Outline platelets.
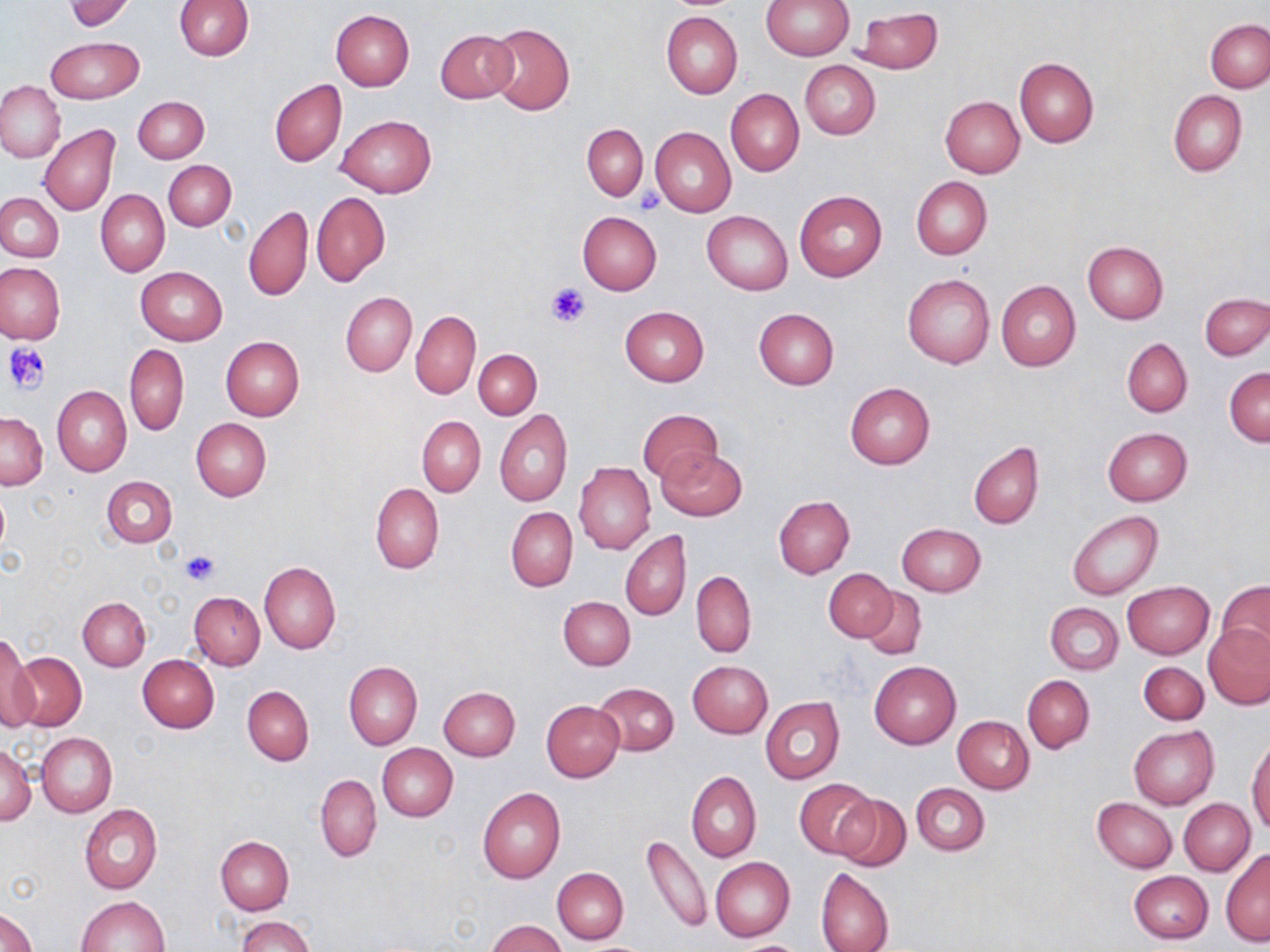

Approximate bounding boxes as (x1, y1, x2, y2) in pixels.
Platelets: (636, 191, 665, 215), (546, 284, 590, 330), (2, 343, 51, 394), (179, 549, 220, 586).

Uninfected red blood cell locations: (760, 0, 853, 60), (65, 1, 134, 31), (174, 1, 253, 61), (330, 9, 415, 91), (853, 9, 943, 74), (662, 11, 742, 98), (1205, 19, 1270, 93), (486, 22, 575, 115), (435, 29, 517, 102), (46, 37, 142, 104), (1014, 56, 1099, 147), (799, 60, 880, 139), (270, 80, 346, 167), (0, 81, 65, 162), (726, 88, 803, 176), (1169, 89, 1247, 176), (133, 97, 208, 163), (940, 97, 1024, 178), (337, 114, 436, 198), (582, 123, 647, 200), (39, 124, 121, 217), (650, 126, 736, 216), (164, 160, 236, 230), (911, 176, 992, 259), (96, 190, 169, 276), (794, 190, 887, 281), (0, 192, 64, 262), (312, 192, 389, 286), (243, 206, 313, 302), (577, 211, 663, 294), (702, 211, 793, 294), (1081, 242, 1167, 324), (0, 263, 64, 343), (135, 266, 228, 346), (903, 273, 995, 369), (996, 279, 1081, 371), (340, 292, 416, 377), (1200, 292, 1270, 361), (620, 306, 709, 386), (754, 308, 839, 389), (411, 310, 480, 399), (221, 336, 304, 421), (1121, 338, 1192, 416), (125, 343, 189, 435), (474, 350, 541, 419), (1225, 367, 1270, 447), (845, 382, 935, 469), (52, 386, 131, 477), (638, 407, 721, 483), (495, 410, 572, 506), (1, 412, 47, 489), (417, 416, 486, 497), (191, 418, 272, 501), (1102, 427, 1192, 506), (968, 441, 1044, 530), (656, 447, 747, 521), (574, 462, 655, 555), (101, 475, 177, 548), (370, 483, 444, 574), (773, 496, 854, 577), (507, 507, 577, 591), (1067, 511, 1163, 600), (896, 523, 985, 597), (621, 530, 691, 622), (259, 560, 340, 653), (825, 568, 897, 642), (691, 571, 756, 656), (1218, 580, 1270, 658), (1122, 581, 1215, 658), (860, 587, 926, 661), (189, 592, 264, 669), (559, 595, 635, 669), (78, 596, 151, 670), (1046, 602, 1123, 674), (1204, 622, 1270, 708), (1, 641, 39, 733), (6, 652, 87, 731), (138, 655, 219, 733), (688, 660, 772, 737), (869, 660, 962, 748), (344, 661, 422, 750), (1138, 662, 1209, 724), (1023, 673, 1094, 753), (593, 682, 678, 756), (242, 686, 315, 765), (438, 686, 520, 761), (760, 696, 845, 784), (541, 700, 625, 782), (952, 715, 1034, 793), (1128, 724, 1219, 809), (36, 732, 116, 817), (1248, 737, 1270, 835), (1, 743, 36, 825), (377, 744, 457, 820), (686, 771, 761, 862), (316, 775, 382, 862), (795, 778, 878, 859), (910, 783, 989, 855), (477, 787, 565, 883), (831, 794, 911, 873), (1092, 797, 1177, 872), (1179, 798, 1254, 875), (80, 804, 162, 893), (640, 833, 711, 934), (216, 837, 294, 914), (1221, 850, 1270, 946), (710, 856, 795, 942), (815, 867, 893, 952), (553, 868, 629, 944), (1129, 871, 1212, 944), (77, 895, 169, 951), (0, 908, 39, 952), (237, 915, 314, 952), (485, 919, 567, 951). Slide-level diagnosis: no evidence of blood parasites. May-Grünwald-Giemsa-stained preparation. 1000x magnification. Image is 1270×952 pixels. Light microscopy. Single field of view. Thin blood smear.